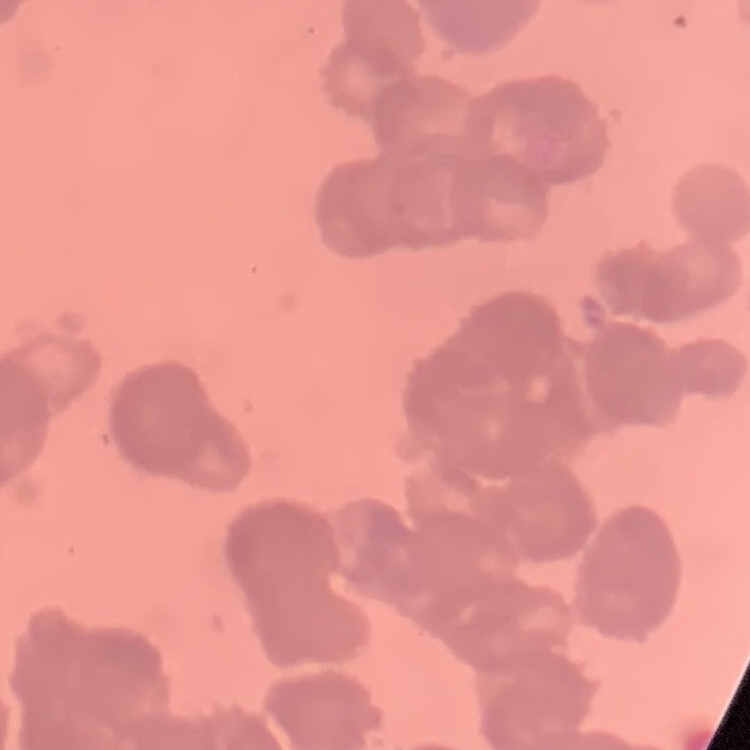

red_blood_cell_morphology: rouleaux formation
preparation: thin blood film
stain: Field's or Giemsa
image_type: square crop of a larger photomicrograph